Assess this cell for malaria.
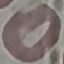

It is uninfected.

Summary:
  - Preparation: thin blood smear
  - Capture: smartphone camera at the microscope eyepiece
  - Image type: automatically extracted cell patch, resized to 64 × 64 pixels
  - Stain: Giemsa